Locate every Plasmodium parasite and every leukocyte.
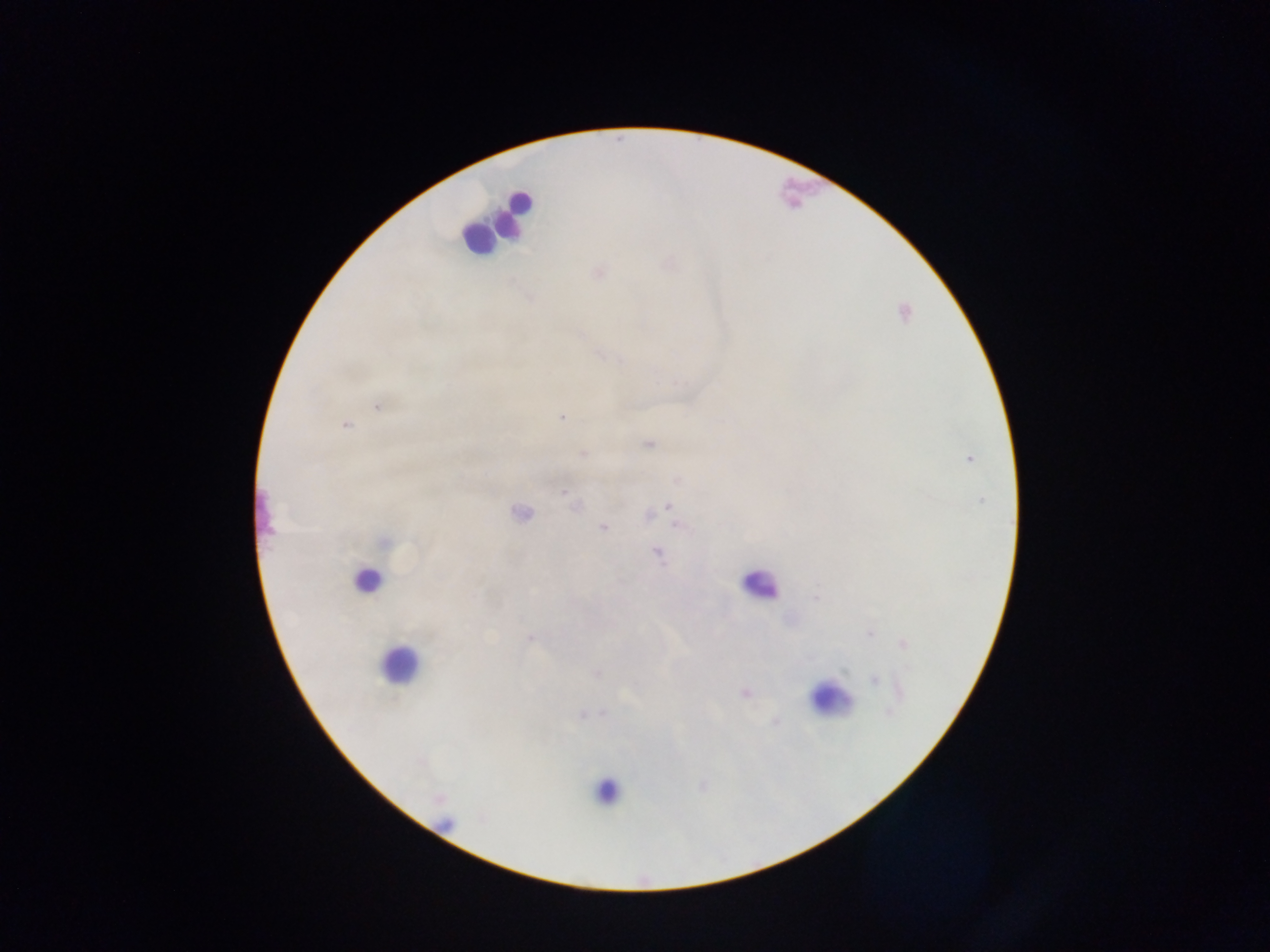
Approximate centers as {x, y} in pixels.
Plasmodium parasites: {599, 273}, {377, 407}, {562, 417}, {345, 426}, {649, 445}, {583, 454}, {969, 459}, {677, 480}, {564, 492}, {981, 500}, {573, 503}, {669, 506}, {520, 514}, {648, 516}, {679, 526}, {604, 527}, {385, 542}, {657, 553}, {816, 598}, {870, 633}, {530, 638}, {903, 643}, {907, 668}, {597, 673}, {875, 680}, {900, 692}, {744, 693}, {889, 712}, {775, 721}.
Leukocytes: {514, 212}, {476, 240}, {365, 580}, {759, 585}, {397, 665}, {830, 699}, {606, 792}.

Summary:
  - Preparation: thick blood smear
  - Country: Ghana
  - Field of view: single
  - Capture: mobile-phone photograph through a microscope
  - Image size: 1270×952 pixels